Classify this cell by malaria status.
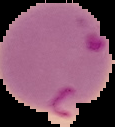
It is parasitized.

Summary:
  - Image type: segmented cell region on a black background
  - Preparation: thin blood film
  - Image size: 115×127 pixels